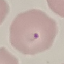
malaria status = parasitized
preparation = thin blood smear
stain = Giemsa
image type = cell patch, automatically extracted from a larger field of view and resized to 64 × 64 pixels
capture = smartphone camera at the microscope eyepiece